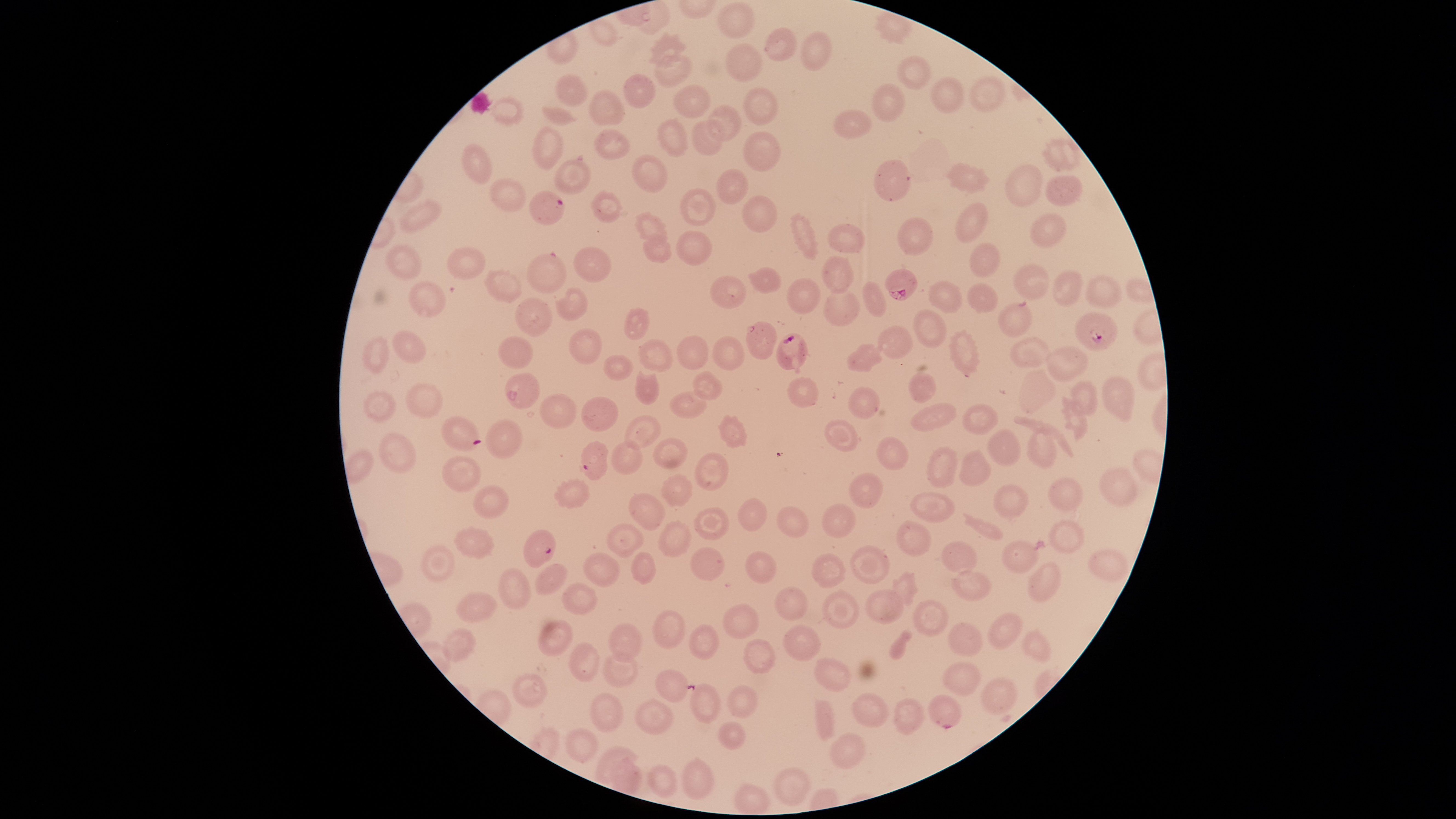
stain = Giemsa
visible region = circular
uninfected red blood cells = approximate bounding boxes as (left, top, right, bottom) in pixels: (717, 2, 754, 40), (875, 11, 912, 46), (588, 18, 618, 47), (764, 27, 798, 62), (648, 30, 688, 68), (800, 31, 832, 72), (726, 42, 763, 82), (653, 54, 693, 88), (896, 56, 931, 92), (554, 72, 587, 108), (623, 73, 656, 108), (969, 76, 1007, 112), (931, 77, 965, 115), (871, 83, 906, 123), (673, 85, 711, 118), (743, 87, 778, 126), (588, 90, 625, 126), (490, 94, 524, 127), (708, 104, 743, 142), (541, 106, 576, 127), (832, 108, 873, 139), (657, 118, 688, 159), (690, 119, 725, 156), (531, 126, 564, 171), (594, 129, 630, 160), (743, 130, 782, 172), (1038, 136, 1082, 172), (461, 142, 492, 185), (630, 152, 670, 195), (554, 158, 592, 197), (874, 160, 911, 202), (944, 162, 991, 194), (1005, 163, 1044, 208), (715, 167, 748, 205), (1045, 175, 1083, 207), (490, 179, 527, 213), (680, 188, 716, 226), (590, 191, 623, 223), (741, 195, 778, 233), (400, 199, 441, 234), (954, 203, 990, 243), (632, 211, 667, 243), (788, 212, 820, 260), (1029, 213, 1066, 247), (897, 217, 934, 257), (827, 223, 866, 255), (675, 230, 713, 267), (641, 233, 671, 264), (969, 243, 1001, 277), (385, 245, 421, 280), (447, 247, 486, 281), (573, 247, 613, 283), (526, 252, 566, 294), (821, 255, 854, 294), (1012, 262, 1049, 301), (483, 267, 523, 303), (747, 267, 782, 295), (1051, 271, 1084, 306), (1085, 274, 1123, 309), (710, 275, 747, 309), (786, 277, 822, 315), (928, 280, 962, 313), (407, 281, 446, 317), (862, 281, 888, 317), (967, 283, 998, 314), (555, 287, 586, 322), (823, 288, 861, 327), (515, 297, 553, 337), (999, 300, 1033, 337), (623, 306, 650, 340), (913, 309, 948, 348), (745, 320, 778, 360), (877, 324, 912, 359), (391, 329, 426, 364), (570, 329, 603, 364), (948, 329, 981, 378), (361, 335, 390, 374), (677, 335, 709, 370), (712, 335, 746, 371), (498, 336, 533, 369), (1010, 336, 1051, 369), (637, 338, 673, 373), (846, 344, 883, 372), (1045, 346, 1088, 382), (603, 354, 634, 381), (1017, 368, 1056, 415), (692, 369, 724, 400), (908, 370, 937, 403), (634, 371, 661, 406), (504, 373, 541, 410), (1102, 374, 1136, 421), (787, 377, 820, 409), (1070, 380, 1098, 416), (406, 382, 445, 418), (847, 385, 881, 420), (362, 389, 397, 423), (670, 390, 706, 419), (539, 392, 576, 428), (1060, 395, 1089, 442), (581, 396, 619, 432), (910, 403, 957, 432), (962, 404, 999, 434), (624, 414, 661, 452), (717, 416, 749, 449), (485, 419, 525, 459), (824, 419, 858, 452), (987, 429, 1022, 467), (378, 432, 417, 474), (1027, 432, 1057, 470), (876, 436, 909, 471), (652, 438, 688, 469), (610, 439, 643, 476), (926, 446, 958, 489), (958, 447, 992, 488), (694, 452, 729, 492), (440, 455, 481, 493), (1100, 468, 1138, 507), (848, 472, 883, 510), (661, 473, 693, 508), (553, 477, 591, 509), (1048, 477, 1083, 512), (991, 482, 1030, 517), (472, 485, 509, 519), (627, 492, 666, 531), (909, 492, 954, 523), (737, 498, 768, 532), (821, 504, 855, 539), (775, 506, 809, 538), (693, 507, 728, 540), (657, 520, 692, 558), (895, 520, 932, 556), (1048, 520, 1085, 554), (606, 523, 644, 559), (453, 526, 496, 560), (1001, 538, 1039, 574), (941, 540, 978, 573), (419, 544, 456, 583), (849, 545, 890, 583), (690, 547, 725, 580), (1088, 549, 1130, 581), (582, 551, 620, 588), (745, 551, 776, 583), (631, 552, 656, 585), (810, 553, 846, 588), (1027, 561, 1061, 603), (536, 563, 568, 594), (496, 567, 531, 609), (951, 568, 993, 601), (890, 571, 920, 606), (560, 583, 598, 616), (774, 586, 807, 621), (822, 589, 861, 628), (864, 589, 905, 625), (455, 592, 498, 623), (912, 599, 949, 637), (723, 604, 761, 639), (652, 610, 686, 648), (987, 612, 1023, 650), (537, 619, 574, 657), (947, 622, 984, 657), (606, 623, 641, 663), (687, 624, 720, 661), (783, 625, 821, 660), (442, 627, 477, 664), (1020, 627, 1051, 663), (743, 639, 776, 675), (568, 643, 600, 681), (602, 653, 638, 688), (813, 658, 851, 693), (943, 661, 980, 696), (655, 670, 687, 703), (509, 673, 547, 709), (979, 678, 1017, 717), (689, 683, 722, 725), (727, 684, 759, 718), (591, 692, 624, 734), (852, 693, 889, 727), (927, 694, 961, 729), (892, 698, 923, 735), (636, 699, 675, 737), (717, 721, 747, 751), (564, 727, 599, 763), (829, 732, 866, 770), (595, 744, 638, 783), (682, 757, 717, 801), (772, 767, 813, 806)
presence = malaria parasites identified
image size = 1456×819 pixels
capture = smartphone photograph through the microscope eyepiece
preparation = thin blood film
field of view = single
parasitized red blood cells = approximate bounding boxes as (left, top, right, bottom) in pixels: (529, 191, 565, 226), (885, 267, 918, 300), (1075, 312, 1117, 351), (776, 332, 811, 374), (440, 415, 482, 452), (579, 441, 608, 481), (523, 529, 556, 570)
species = Plasmodium falciparum